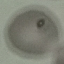
Result: no malaria parasites seen. Automatically extracted cell patch, resized to 64 × 64 pixels. Acquired by smartphone through the microscope eyepiece. Thin blood smear. Giemsa-stained preparation.